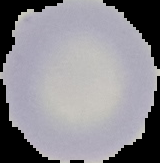
Summary:
  - Image type: segmented cell region with the area outside set to black
  - Image size: 160×163 pixels
  - Result: negative for Plasmodium parasites
  - Preparation: thin blood smear